Report the malaria status of this cell.
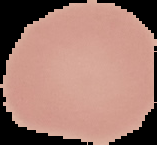

Uninfected.

Summary:
  - Preparation: thin blood smear
  - Image size: 157×145 pixels
  - Image type: segmented cell region with the area outside set to black